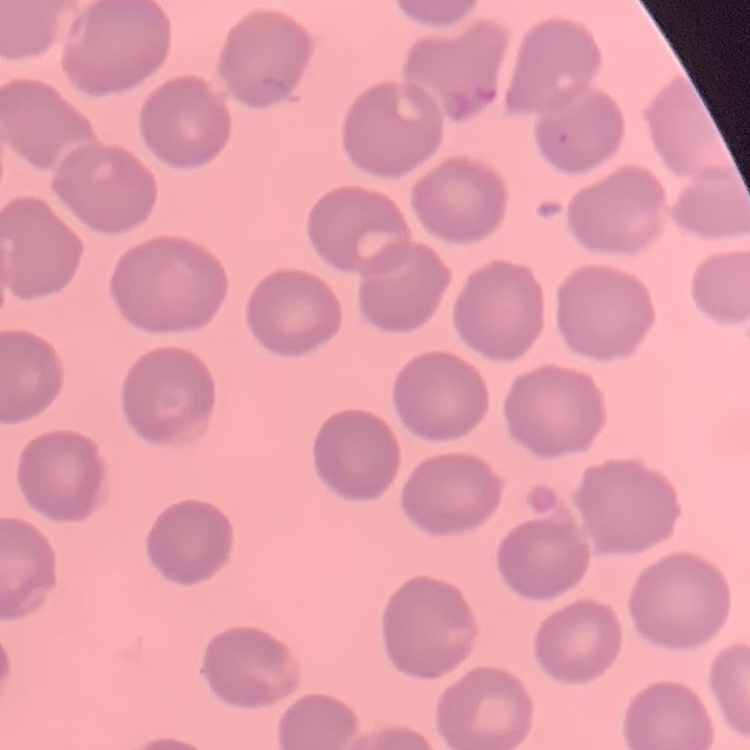

Summary:
  - Red blood cell morphology: no rouleaux formation
  - Image type: square crop of a larger photomicrograph
  - Stain: Field's or Giemsa
  - Preparation: thin blood film